Name the parasite shown.
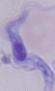
This is a trypanosome.

Photomicrograph. Captured at 1000x magnification.